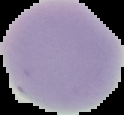

Summary:
  - Preparation: thin blood smear
  - Image type: segmented cell region on a black background
  - Malaria status: uninfected
  - Image size: 124×115 pixels